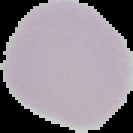
Image is 133×133 pixels. From a thin blood film. Result: no Plasmodium parasites detected. Cell region segmented out of the field of view; the surrounding area is masked to black.